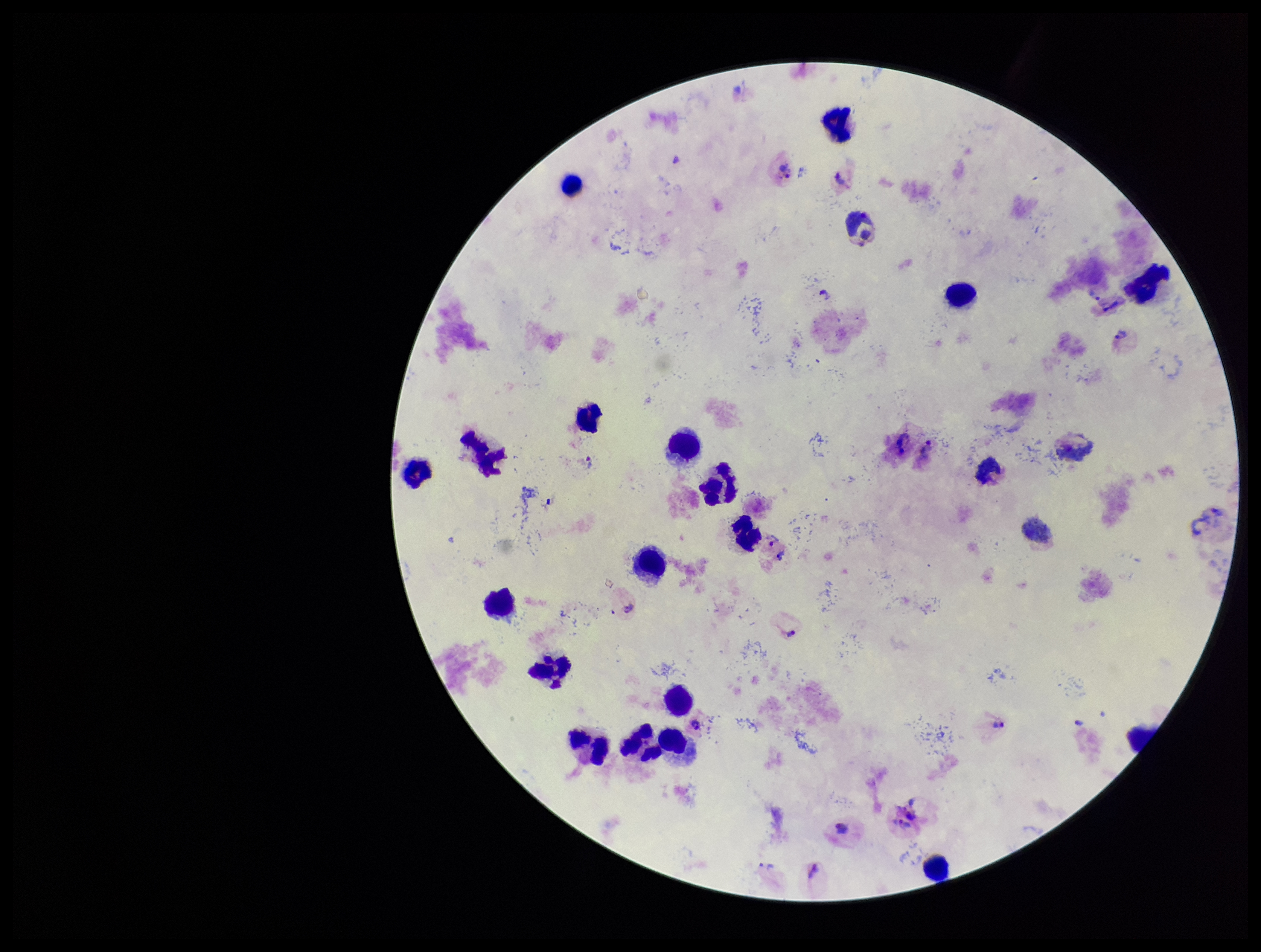

species reported for this patient = Plasmodium vivax
preparation = thick smear
patient malaria status = infected
leukocyte count = 22
field of view = one from this slide
Plasmodium parasites = seen
stain = Giemsa
parasite count = 10
capture = smartphone photograph through the microscope eyepiece
image size = 1261×952 pixels